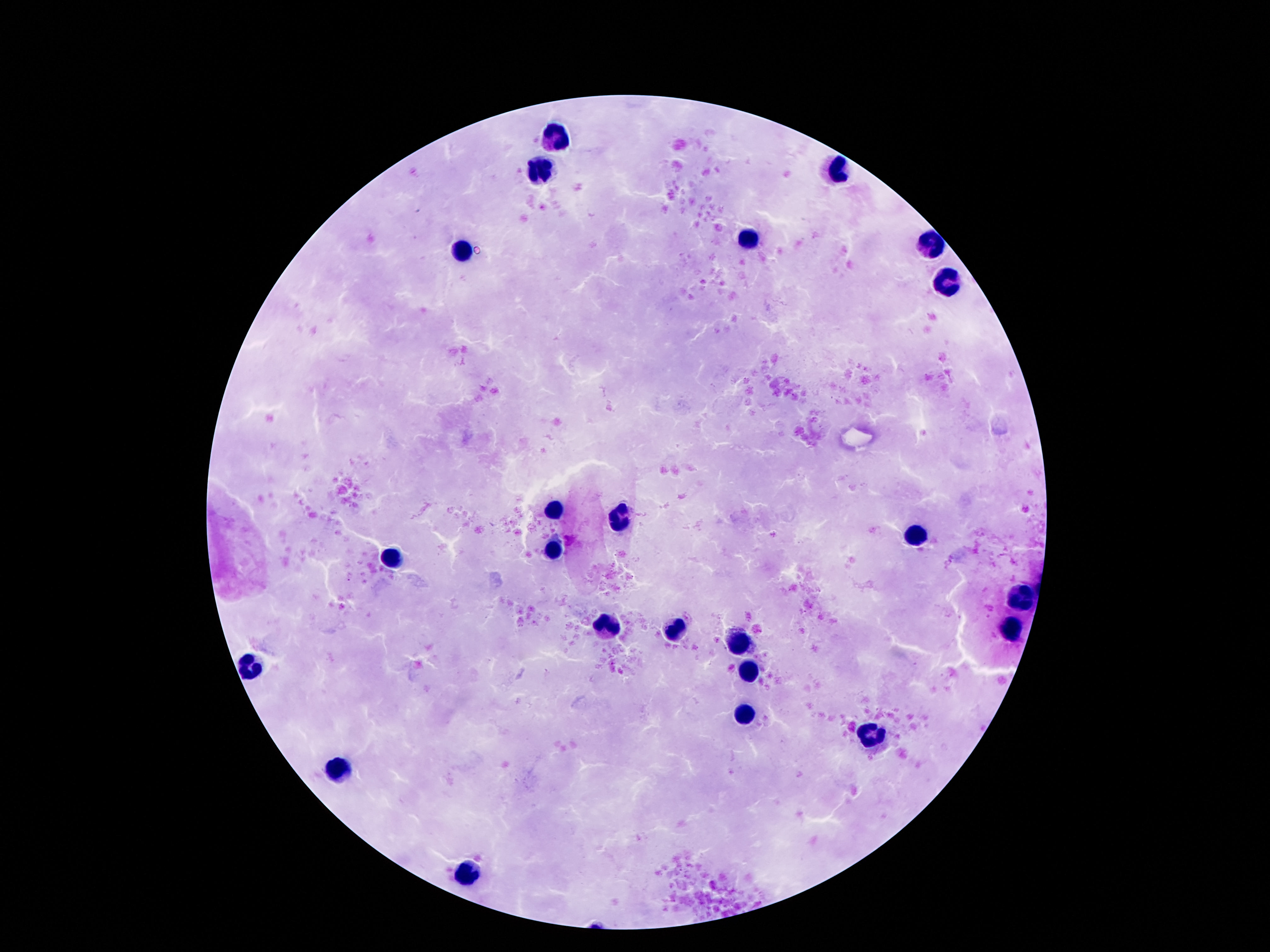
Approximate object centers, in pixels from the top-left corner.
Summary:
  - Leukocyte locations: (x=557, y=136), (x=542, y=169), (x=838, y=169), (x=746, y=241), (x=933, y=245), (x=464, y=251), (x=943, y=286), (x=555, y=510), (x=620, y=518), (x=916, y=535), (x=552, y=548), (x=386, y=556), (x=1021, y=600), (x=607, y=626), (x=1012, y=628), (x=674, y=630), (x=739, y=645), (x=250, y=666), (x=752, y=668), (x=746, y=714), (x=870, y=735), (x=338, y=771), (x=468, y=870)
  - Magnification: 100x
  - Patient malaria status: not infected
  - Image size: 1270×952 pixels
  - Capture: smartphone camera through the microscope eyepiece
  - Field of view: one from this slide
  - Stain: Giemsa
  - Preparation: thick blood film